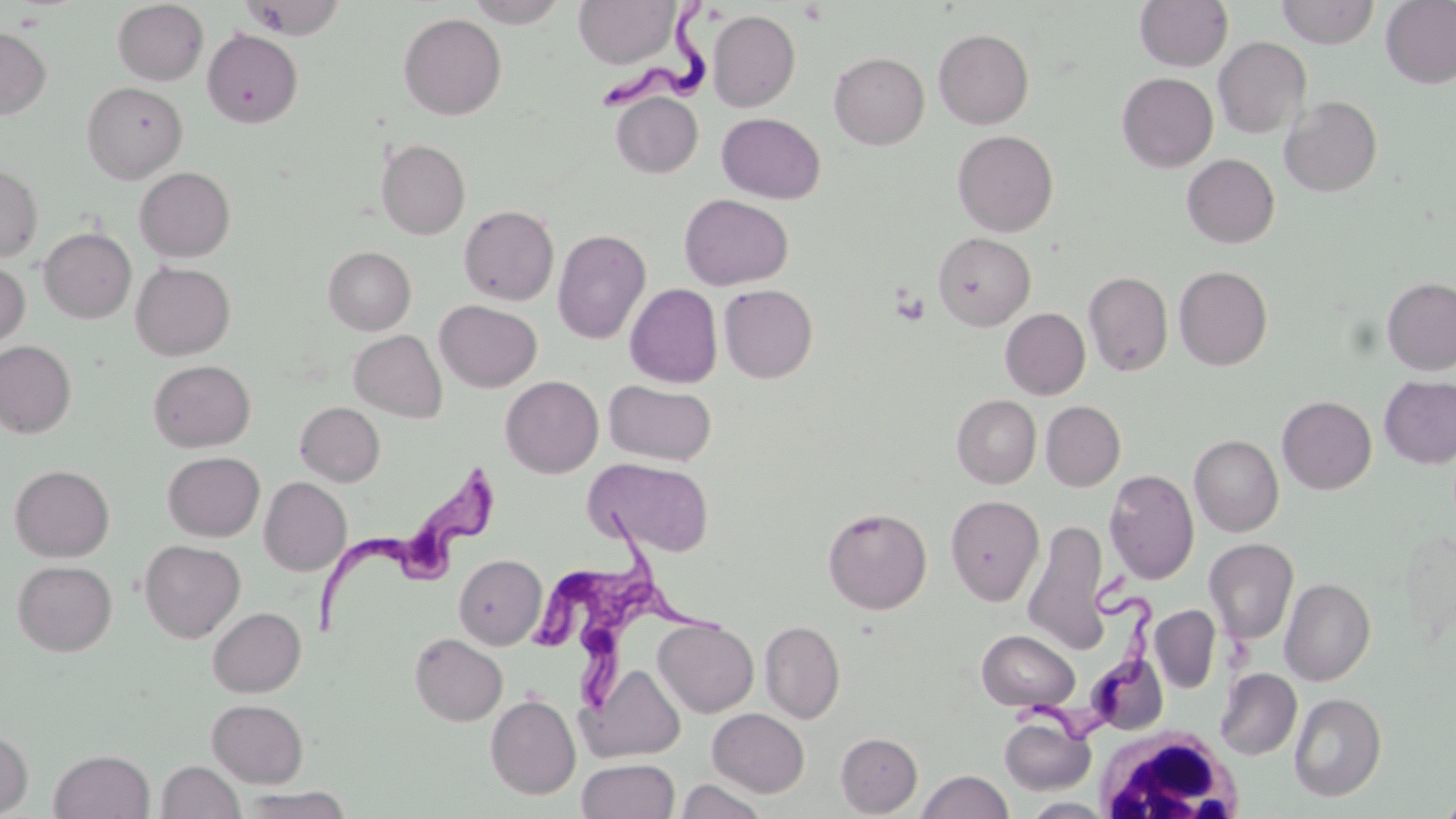

slide-level diagnosis = Trypanosoma brucei
platelet locations = approximate bounding boxes as (x1, y1, x2, y2) in pixels: (799, 3, 829, 25), (891, 288, 930, 327)
image size = 1456×819 pixels
field of view = single
preparation = thin blood smear
Trypanosoma brucei locations = approximate bounding boxes as (x1, y1, x2, y2) in pixels: (599, 2, 721, 117), (310, 464, 497, 633), (539, 506, 666, 647), (579, 576, 735, 709), (1016, 580, 1160, 743)
white blood cell locations = approximate bounding boxes as (x1, y1, x2, y2) in pixels: (1093, 727, 1247, 819)
magnification = 1000x
stain = May-Grünwald-Giemsa
modality = light microscopy
uninfected red blood cell locations = approximate bounding boxes as (x1, y1, x2, y2) in pixels: (239, 0, 347, 39), (464, 0, 569, 27), (573, 0, 680, 68), (1134, 0, 1233, 71), (1276, 0, 1379, 48), (112, 1, 209, 85), (1381, 1, 1456, 88), (708, 9, 800, 112), (398, 13, 507, 120), (0, 27, 51, 119), (202, 28, 303, 128), (933, 28, 1034, 129), (1213, 37, 1311, 139), (829, 52, 929, 149), (1117, 72, 1218, 172), (82, 81, 187, 182), (611, 92, 703, 178), (1280, 96, 1382, 197), (717, 112, 825, 204), (952, 130, 1058, 237), (376, 138, 470, 239), (1182, 153, 1280, 247), (0, 164, 43, 262), (134, 166, 236, 262), (679, 194, 793, 290), (459, 205, 559, 305), (39, 227, 136, 323), (553, 229, 651, 344), (933, 232, 1035, 330), (323, 246, 416, 334), (0, 260, 30, 352), (131, 262, 236, 360), (144, 262, 245, 451), (1174, 265, 1273, 370), (1083, 272, 1173, 376), (1382, 278, 1456, 375), (625, 283, 723, 388), (719, 284, 818, 383), (434, 300, 542, 392), (1000, 308, 1090, 399), (349, 330, 447, 422), (0, 340, 76, 438), (148, 359, 256, 452), (500, 375, 603, 478), (1379, 375, 1456, 468), (604, 380, 716, 465), (951, 395, 1041, 488), (1277, 395, 1377, 494), (1041, 401, 1125, 490), (295, 402, 384, 486), (1189, 434, 1284, 536), (162, 451, 265, 541), (588, 458, 715, 557), (9, 464, 115, 561), (1104, 469, 1199, 584), (259, 477, 351, 575), (945, 494, 1044, 606), (823, 507, 932, 614), (1023, 519, 1111, 655), (1400, 528, 1456, 646), (1204, 538, 1298, 643), (139, 540, 245, 642), (454, 554, 547, 649), (12, 560, 117, 656), (1280, 578, 1375, 686), (1150, 605, 1220, 693), (208, 607, 306, 696), (653, 618, 758, 716), (760, 620, 845, 724), (976, 629, 1080, 712), (410, 633, 507, 725), (583, 663, 686, 762), (1215, 668, 1302, 760), (1289, 692, 1386, 801), (485, 693, 581, 800), (206, 698, 309, 787), (707, 708, 809, 797), (999, 715, 1096, 795), (0, 729, 32, 816), (836, 732, 922, 816), (49, 749, 154, 819), (577, 758, 679, 818), (157, 761, 244, 819), (917, 770, 1014, 819), (676, 777, 769, 818), (239, 787, 355, 818), (1438, 793, 1456, 818), (1021, 797, 1113, 818)